Comment on the morphology of the erythrocytes.
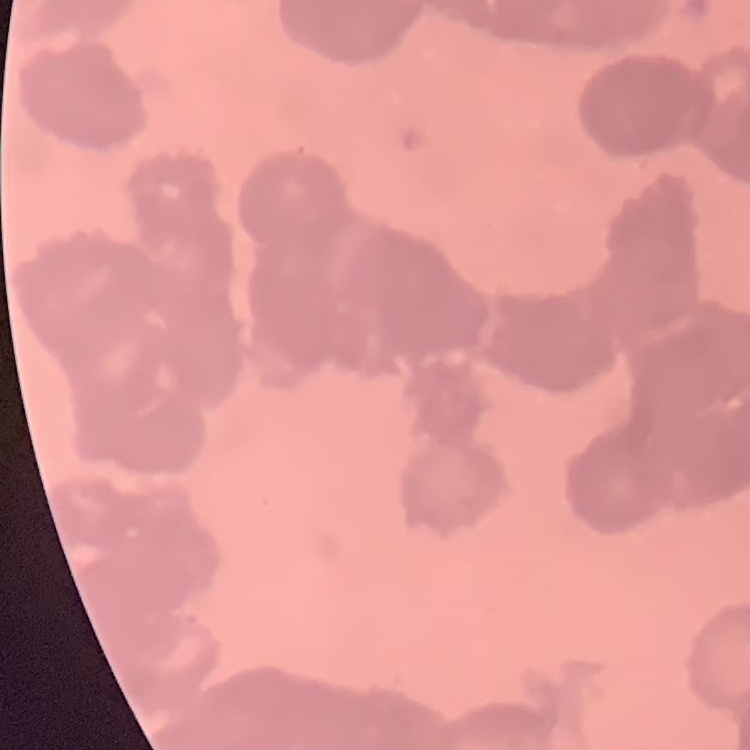

Rouleaux formation.

image type = one tile cut from a larger photomicrograph
preparation = thin blood film
stain = Field's or Giemsa